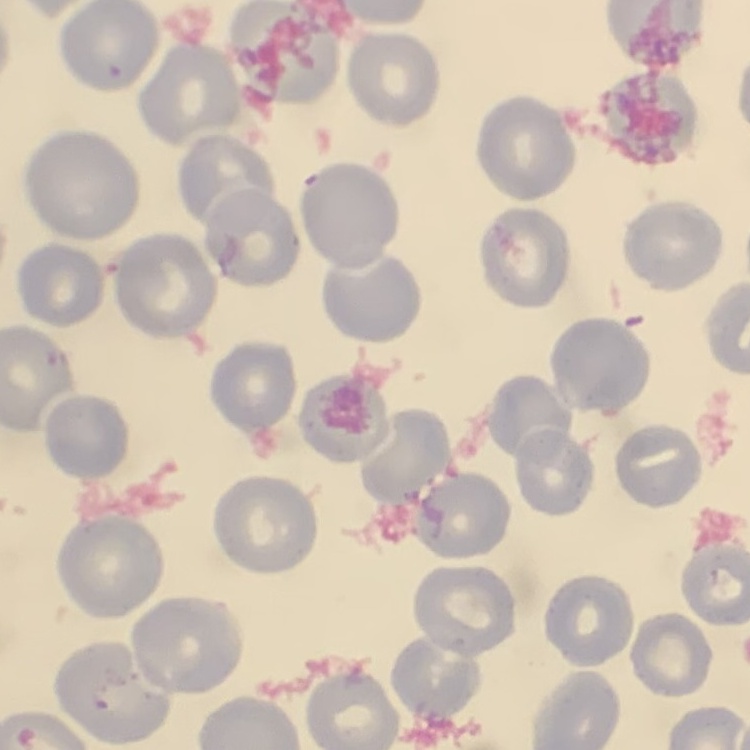
Summary:
  - Red blood cell morphology: no rouleaux formation
  - Image type: one tile cut from a larger photomicrograph
  - Stain: Field's or Giemsa
  - Preparation: thin peripheral smear